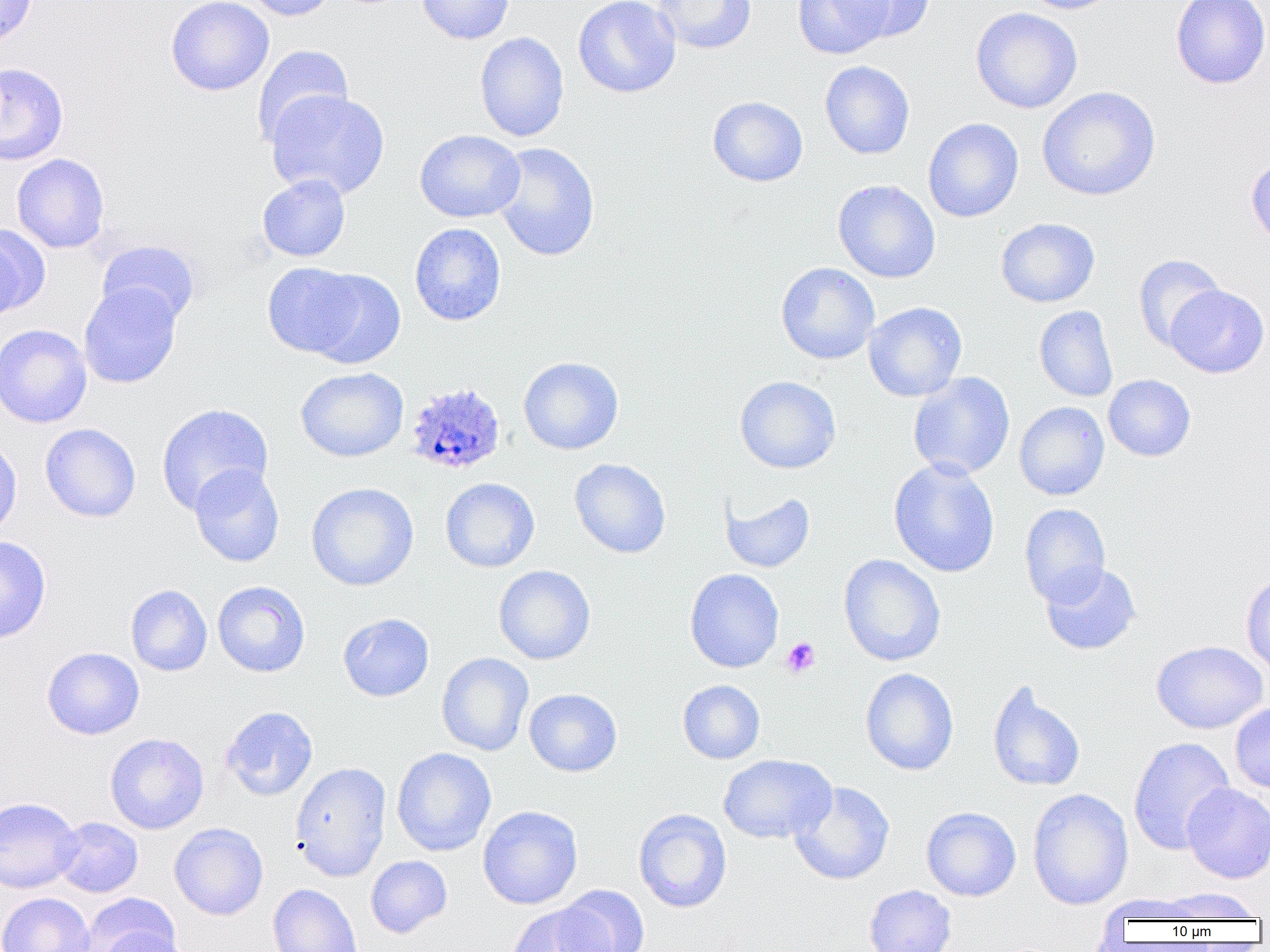

slide-level diagnosis = Plasmodium ovale
magnification = 1000x
Plasmodium ovale-infected red blood cell locations = approximate bounding boxes as (x1,y1)-(x2,y2) corner pairs in pixels: (405,382)-(506,476)
image size = 1270×952 pixels
uninfected red blood cell locations = approximate bounding boxes as (x1,y1)-(x2,y2) corner pairs in pixels: (0,0)-(38,49), (166,0)-(274,96), (241,0)-(335,21), (416,0)-(514,44), (573,0)-(681,98), (652,0)-(757,54), (792,0)-(893,59), (837,0)-(936,43), (1018,0)-(1123,14), (1170,0)-(1270,89), (971,7)-(1082,114), (475,31)-(569,142), (252,44)-(353,148), (820,60)-(915,159), (0,63)-(68,165), (1037,86)-(1160,201), (265,89)-(390,200), (707,96)-(808,186), (923,118)-(1023,223), (415,130)-(525,222), (492,142)-(600,261), (12,153)-(110,253), (1245,153)-(1270,250), (258,174)-(351,262), (832,180)-(940,283), (996,217)-(1100,308), (410,223)-(506,326), (0,224)-(49,317), (96,240)-(201,327), (1133,254)-(1226,352), (262,262)-(367,359), (776,262)-(880,364), (304,269)-(406,368), (79,283)-(183,388), (1165,285)-(1269,378), (863,301)-(967,402), (1034,305)-(1118,402), (1,323)-(92,428), (518,356)-(624,455), (295,367)-(408,462), (908,372)-(1015,480), (1103,374)-(1196,461), (735,376)-(841,474), (1014,401)-(1109,500), (156,403)-(273,514), (41,423)-(141,522), (0,435)-(22,538), (569,458)-(671,558), (889,458)-(1000,578), (189,464)-(285,567), (440,477)-(539,572), (306,482)-(418,591), (719,489)-(815,573), (1020,503)-(1111,607), (0,535)-(51,644), (838,554)-(946,667), (852,555)-(951,775), (1040,562)-(1141,655), (493,565)-(596,665), (684,568)-(784,673), (1241,573)-(1270,676), (213,581)-(310,677), (125,584)-(212,676), (338,612)-(434,702), (1152,640)-(1268,734), (42,647)-(144,740), (436,652)-(534,756), (860,668)-(959,776), (677,680)-(765,764), (987,681)-(1086,792), (524,688)-(622,777), (1229,702)-(1270,794), (221,706)-(318,801), (105,732)-(209,834), (1128,736)-(1235,856), (392,747)-(496,856), (718,754)-(835,844), (290,762)-(391,881), (789,781)-(894,885), (1182,783)-(1270,884), (1027,788)-(1134,910), (0,796)-(82,893), (477,805)-(583,909), (921,806)-(1021,901), (633,808)-(732,913), (53,816)-(143,897), (169,822)-(269,920), (365,855)-(452,938), (268,884)-(363,952), (555,885)-(650,952), (863,885)-(956,952), (1155,887)-(1263,921), (0,892)-(95,952), (80,893)-(181,952), (505,903)-(611,952), (97,930)-(195,952)
preparation = thin blood smear
modality = optical microscopy
field of view = single
platelet locations = approximate bounding boxes as (x1,y1)-(x2,y2) corner pairs in pixels: (781,637)-(820,678)